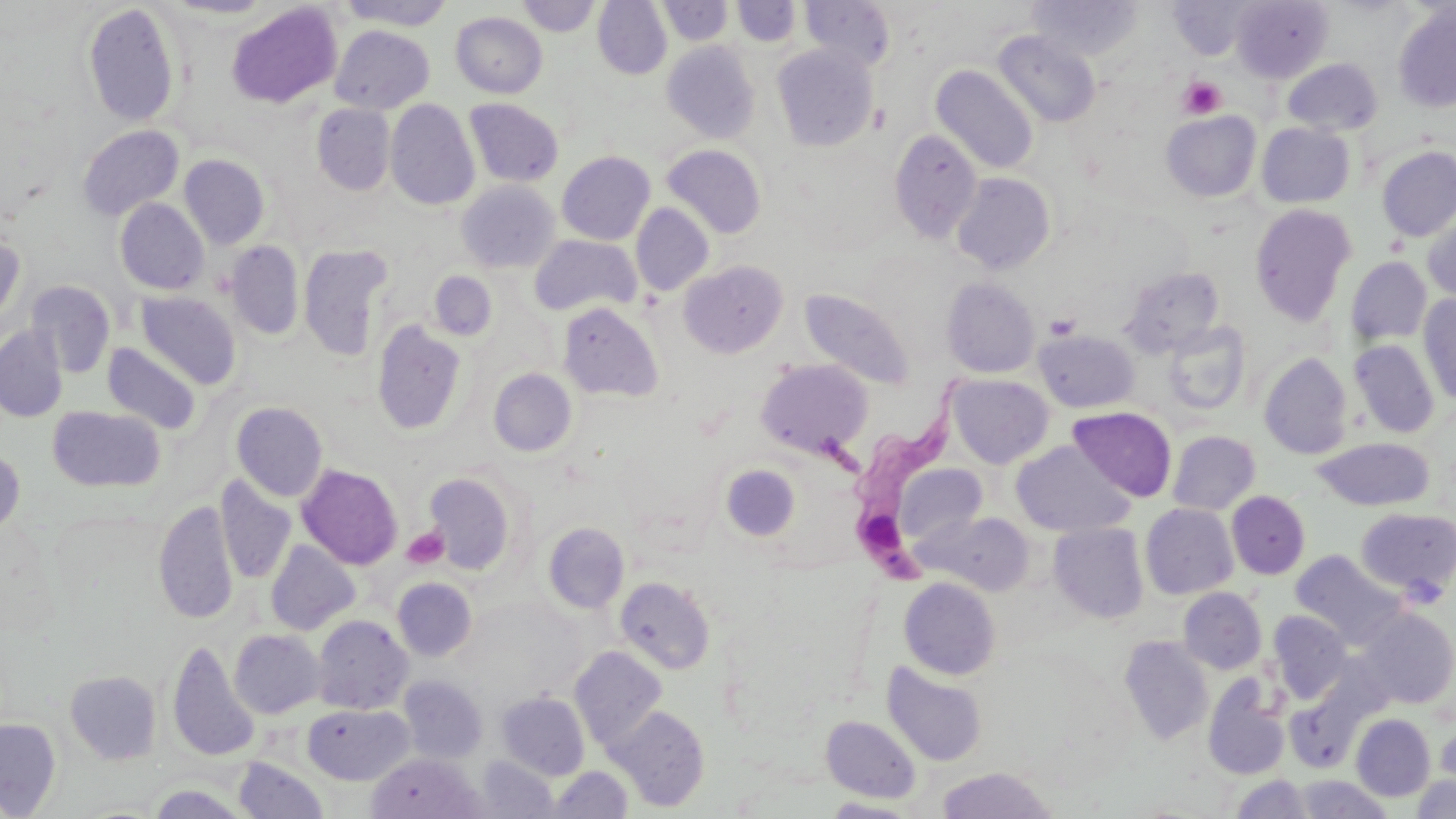
slide-level diagnosis = Trypanosoma brucei
preparation = thin blood film
uninfected red blood cell locations = approximate bounding boxes as (x1,y1)-(x2,y2) corner pairs in pixels: (162,0)-(278,20), (516,0)-(600,37), (593,0)-(672,79), (658,0)-(733,45), (800,0)-(896,73), (1027,0)-(1143,61), (1231,0)-(1333,83), (336,1)-(457,30), (731,1)-(801,46), (1170,1)-(1255,60), (226,2)-(342,109), (83,3)-(180,128), (1392,4)-(1456,113), (451,11)-(547,98), (330,25)-(434,114), (992,30)-(1101,129), (662,41)-(760,144), (772,45)-(878,151), (1282,58)-(1383,136), (931,65)-(1039,175), (385,99)-(480,211), (464,99)-(564,187), (312,104)-(395,195), (1161,110)-(1261,201), (1256,122)-(1355,208), (77,125)-(184,220), (889,130)-(982,244), (661,144)-(766,239), (1376,146)-(1456,242), (557,151)-(655,244), (179,154)-(269,249), (952,173)-(1055,274), (457,181)-(559,273), (115,198)-(209,295), (630,203)-(713,296), (1249,204)-(1357,326), (1422,213)-(1456,302), (0,229)-(26,325), (529,235)-(641,318), (226,241)-(304,340), (298,245)-(394,361), (1346,257)-(1432,344), (679,261)-(787,358), (1120,265)-(1225,357), (429,271)-(497,341), (941,277)-(1040,378), (25,280)-(116,377), (800,288)-(915,389), (136,291)-(241,390), (1418,294)-(1456,405), (558,302)-(663,403), (372,319)-(467,435), (1163,322)-(1251,415), (0,326)-(68,422), (1034,329)-(1139,413), (1349,339)-(1440,438), (103,343)-(202,434), (1259,352)-(1353,459), (756,358)-(873,459), (489,368)-(577,457), (947,374)-(1054,468), (231,402)-(328,502), (48,407)-(165,492), (1069,407)-(1176,502), (1167,431)-(1260,515), (1312,437)-(1434,512), (1012,441)-(1133,537), (0,448)-(25,538), (297,464)-(402,570), (720,464)-(801,542), (892,464)-(988,549), (423,472)-(517,575), (215,476)-(296,584), (1226,491)-(1310,579), (154,500)-(239,623), (1140,504)-(1238,599), (1355,508)-(1456,600), (920,510)-(1036,596), (543,522)-(630,613), (1049,523)-(1148,624), (266,540)-(359,635), (1291,550)-(1404,648), (392,577)-(477,661), (615,577)-(715,674), (899,577)-(1001,680), (1178,587)-(1267,674), (1357,608)-(1456,708), (1268,610)-(1352,702), (312,615)-(412,714), (230,629)-(326,718), (1119,636)-(1213,745), (167,641)-(261,761), (569,647)-(668,751), (882,661)-(987,767), (65,670)-(161,764), (399,675)-(488,764), (1203,676)-(1290,780), (497,692)-(589,779), (1286,692)-(1363,773), (303,704)-(413,784), (609,706)-(709,811), (1351,713)-(1436,801), (821,715)-(921,803), (0,717)-(61,816), (1435,722)-(1456,789), (366,752)-(484,818), (475,755)-(559,818), (233,758)-(328,818), (549,765)-(633,818), (935,767)-(1059,818), (1230,774)-(1314,818), (1412,774)-(1456,819), (1294,775)-(1393,819), (146,784)-(250,819), (822,797)-(921,818)
modality = light microscopy
magnification = 1000x
platelet locations = approximate bounding boxes as (x1,y1)-(x2,y2) corner pairs in pixels: (1177,76)-(1226,118), (1044,313)-(1081,341), (401,527)-(448,569)
image size = 1456×819 pixels
stain = May-Grünwald-Giemsa
Trypanosoma brucei locations = approximate bounding boxes as (x1,y1)-(x2,y2) corner pairs in pixels: (843,373)-(968,588)
field of view = single